Identify the blood parasite species.
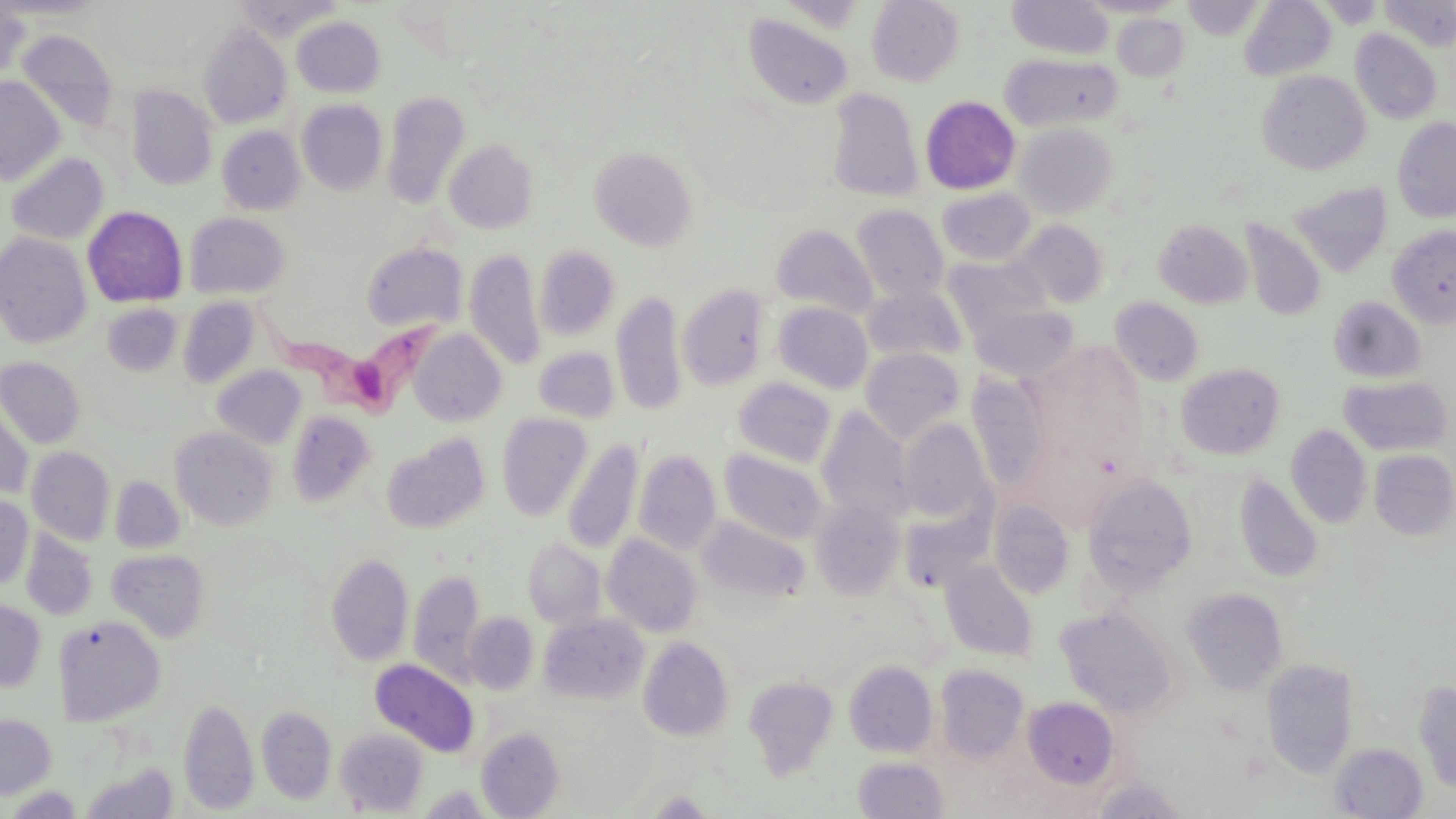

Trypanosoma brucei.

{
  "field_of_view": "single",
  "trypanosoma_brucei_locations": "approximate bounding boxes as (x1, y1, x2, y2) in pixels: (252, 299, 446, 416)",
  "stain": "May-Grünwald-Giemsa",
  "magnification": "1000x",
  "image_size": "1456×819 pixels",
  "modality": "optical microscopy",
  "uninfected_red_blood_cell_locations": "approximate bounding boxes as (x1, y1, x2, y2) in pixels: (0, 0, 107, 19), (231, 0, 344, 40), (866, 0, 965, 87), (1006, 0, 1114, 59), (1079, 0, 1184, 17), (1182, 0, 1265, 40), (1239, 0, 1337, 81), (1378, 0, 1456, 50), (0, 2, 30, 84), (743, 13, 854, 110), (1112, 14, 1190, 81), (291, 16, 386, 97), (198, 23, 293, 129), (16, 29, 119, 133), (1350, 29, 1442, 125), (1000, 53, 1122, 133), (1257, 70, 1372, 175), (0, 77, 65, 185), (127, 85, 218, 190), (826, 87, 924, 202), (381, 90, 471, 211), (920, 95, 1020, 195), (297, 99, 388, 195), (1393, 117, 1456, 223), (1014, 122, 1119, 219), (216, 126, 305, 215), (444, 139, 539, 233), (589, 145, 697, 250), (5, 152, 109, 246), (1288, 181, 1394, 277), (937, 187, 1036, 266), (851, 205, 949, 302), (82, 206, 187, 308), (184, 212, 291, 300), (1154, 218, 1252, 309), (1241, 218, 1326, 322), (1015, 219, 1109, 308), (771, 224, 878, 319), (1387, 224, 1456, 329), (0, 233, 93, 349), (360, 242, 467, 333), (535, 246, 621, 341), (465, 248, 545, 370), (941, 255, 1049, 341), (677, 283, 772, 391), (862, 285, 968, 365), (611, 290, 687, 416), (1328, 296, 1427, 384), (1111, 297, 1204, 387), (178, 298, 260, 389), (774, 302, 873, 394), (101, 303, 182, 377), (971, 304, 1079, 382), (409, 329, 506, 426), (533, 346, 619, 423), (860, 347, 966, 444), (0, 357, 86, 448), (1176, 363, 1286, 460), (212, 365, 306, 450), (967, 374, 1053, 497), (1339, 375, 1452, 456), (733, 377, 837, 467), (1, 399, 34, 498), (816, 407, 915, 525), (286, 410, 376, 507), (497, 413, 592, 521), (898, 419, 993, 526), (1285, 424, 1372, 528), (170, 426, 279, 531), (382, 434, 490, 534), (562, 439, 643, 555), (1019, 440, 1121, 530), (27, 447, 116, 545), (719, 448, 829, 544), (634, 449, 722, 555), (1369, 449, 1456, 540), (1234, 473, 1324, 583), (1083, 475, 1199, 595), (109, 476, 185, 553), (0, 496, 33, 589), (810, 497, 906, 600), (989, 498, 1075, 599), (898, 501, 994, 593), (696, 515, 810, 607), (21, 529, 98, 621), (602, 534, 703, 637), (523, 538, 606, 629), (107, 549, 209, 642), (326, 552, 414, 667), (941, 561, 1039, 662), (409, 568, 486, 682), (1182, 587, 1289, 695), (0, 599, 46, 692), (1055, 606, 1178, 719), (464, 612, 538, 694), (538, 613, 650, 705), (53, 616, 166, 726), (638, 637, 734, 741), (370, 659, 479, 757), (844, 660, 938, 757), (1260, 660, 1359, 778), (934, 664, 1030, 763), (744, 675, 839, 781), (1413, 679, 1456, 794), (1022, 696, 1120, 788), (179, 698, 259, 814), (256, 705, 337, 804), (0, 713, 56, 798), (476, 726, 566, 818), (336, 729, 428, 815), (1330, 742, 1428, 818), (853, 756, 948, 818), (82, 762, 179, 819), (1090, 777, 1191, 819), (417, 784, 496, 817), (4, 786, 84, 818), (646, 790, 715, 817)",
  "preparation": "thin blood smear"
}